Comment on the morphology of the erythrocytes.
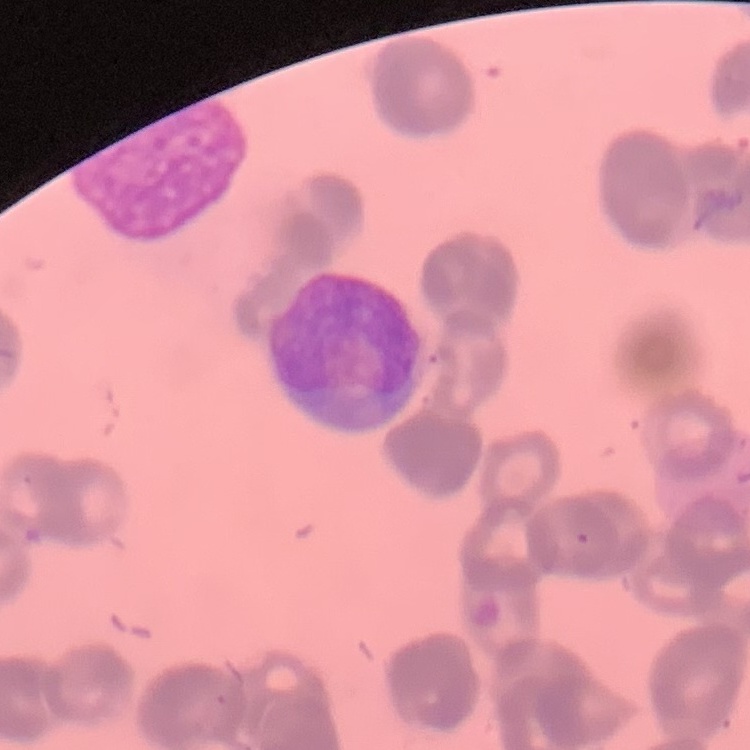

Rouleaux formation.

Summary:
  - Stain: Field's or Giemsa
  - Preparation: thin blood film
  - Image type: square crop of a larger photomicrograph